Name the parasite shown.
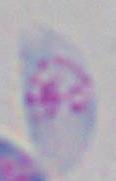

Toxoplasma gondii.

Micrograph. Captured at 1000x magnification.